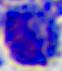 Photomicrograph. 400x magnification. A white blood cell is shown.